Describe the morphology of the erythrocytes.
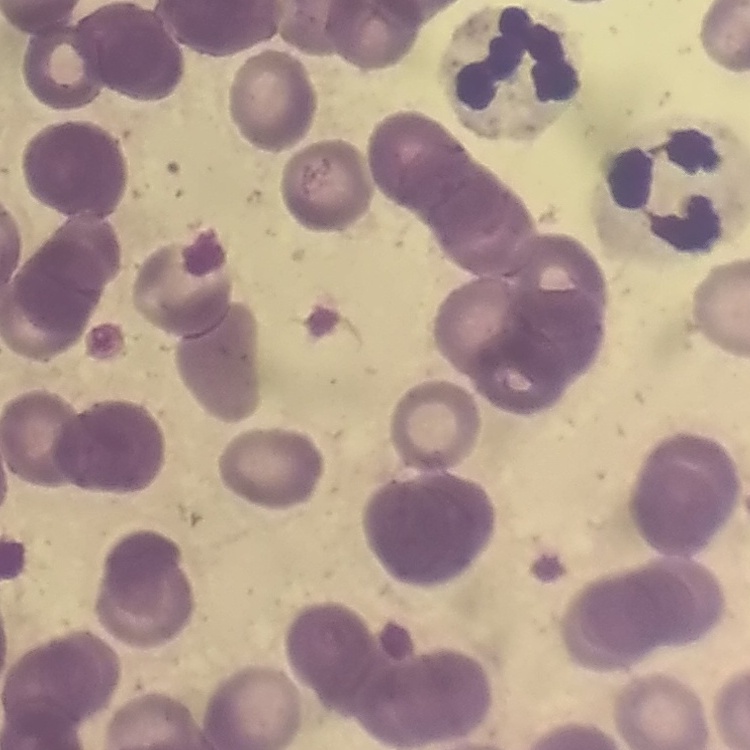
Rouleaux formation.

Summary:
  - Stain: Field's or Giemsa
  - Image type: square crop of a larger photomicrograph
  - Preparation: thin blood film